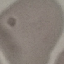

result: no malaria parasites detected
stain: Giemsa
preparation: thin blood smear
capture: smartphone camera at the microscope eyepiece
image_type: automatically extracted cell patch, resized to 64 × 64 pixels